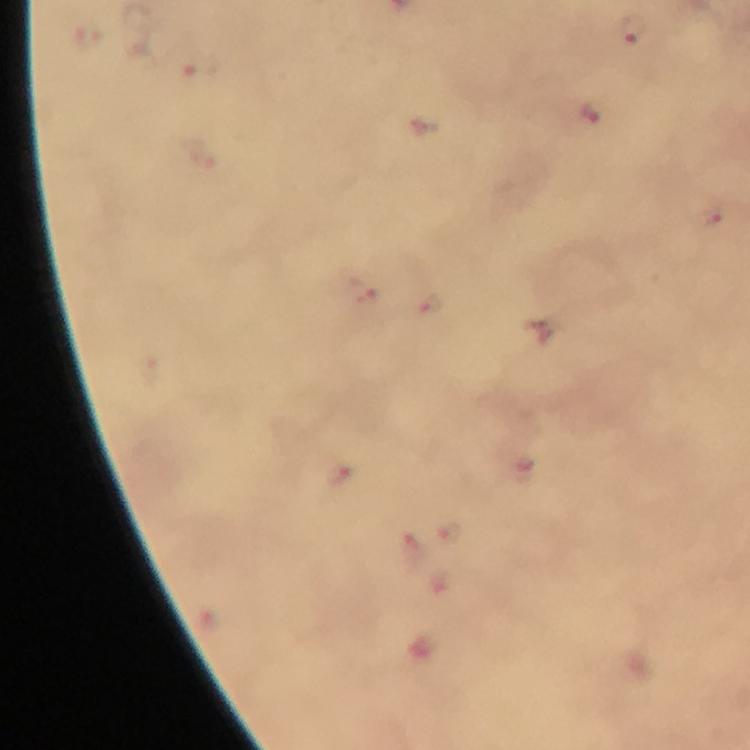

preparation = thick blood film
context = from a diagnostic examination for malaria
stain = Giemsa
malaria parasite locations = approximate centers as [x, y] in pixels: [636, 31], [201, 66], [590, 115], [428, 305]
capture = smartphone mounted on the microscope
cropped from = a single field of view
magnification = 100x
immersion oil = applied
image size = 750×750 pixels